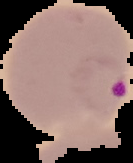
Summary:
  - Image size: 133×163 pixels
  - Result: Plasmodium parasites identified
  - Preparation: thin blood smear
  - Image type: cell region segmented out of the field of view; surrounding area masked to black